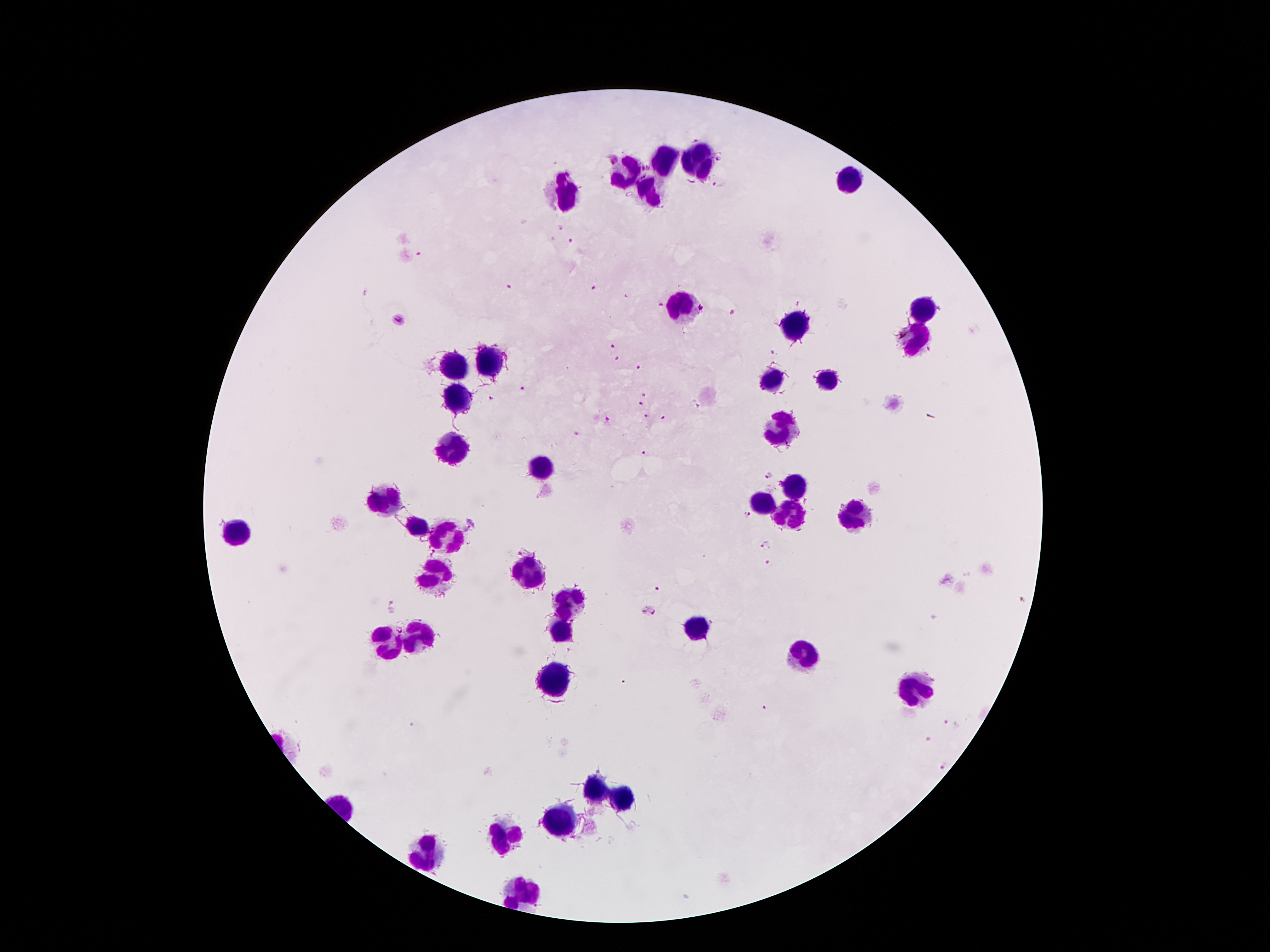
Approximate object centers, in pixels from the top-left corner.
Summary:
  - Leukocyte locations: (x=664, y=160), (x=698, y=163), (x=630, y=174), (x=850, y=178), (x=650, y=192), (x=569, y=197), (x=677, y=307), (x=920, y=312), (x=793, y=326), (x=918, y=339), (x=488, y=362), (x=456, y=367), (x=827, y=376), (x=774, y=381), (x=461, y=397), (x=781, y=430), (x=449, y=447), (x=538, y=467), (x=797, y=483), (x=386, y=501), (x=764, y=502), (x=788, y=515), (x=853, y=517), (x=416, y=526), (x=239, y=532), (x=446, y=534), (x=527, y=571), (x=433, y=573), (x=568, y=601), (x=697, y=627), (x=560, y=631), (x=416, y=636), (x=385, y=646), (x=799, y=653), (x=555, y=678), (x=913, y=691), (x=598, y=790), (x=627, y=799), (x=564, y=818), (x=508, y=836), (x=430, y=855), (x=521, y=890)
  - Malaria parasite locations: (x=613, y=159), (x=719, y=159), (x=718, y=184), (x=561, y=227), (x=570, y=240), (x=420, y=255), (x=511, y=286), (x=595, y=287), (x=625, y=297), (x=797, y=303), (x=660, y=304), (x=703, y=308), (x=733, y=311), (x=400, y=320), (x=611, y=347), (x=772, y=352), (x=616, y=358), (x=637, y=367), (x=524, y=389), (x=643, y=393), (x=490, y=398), (x=694, y=403), (x=640, y=404), (x=645, y=415), (x=661, y=417), (x=609, y=420), (x=577, y=433), (x=645, y=453), (x=769, y=476), (x=746, y=516), (x=766, y=545), (x=526, y=548), (x=768, y=561), (x=660, y=590), (x=396, y=605), (x=646, y=610), (x=765, y=708), (x=947, y=723), (x=926, y=740), (x=942, y=768)
  - Stain: Giemsa
  - Field of view: one from this slide
  - Capture: smartphone through the microscope eyepiece
  - Magnification: 100x
  - Patient malaria status: positive for Plasmodium falciparum
  - Image size: 1270×952 pixels
  - Preparation: thick peripheral-blood smear